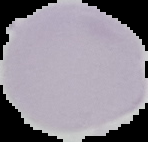 Malaria status: uninfected. From a thin blood film. Image is 148×142 pixels. The area outside the segmented cell region is set to black.